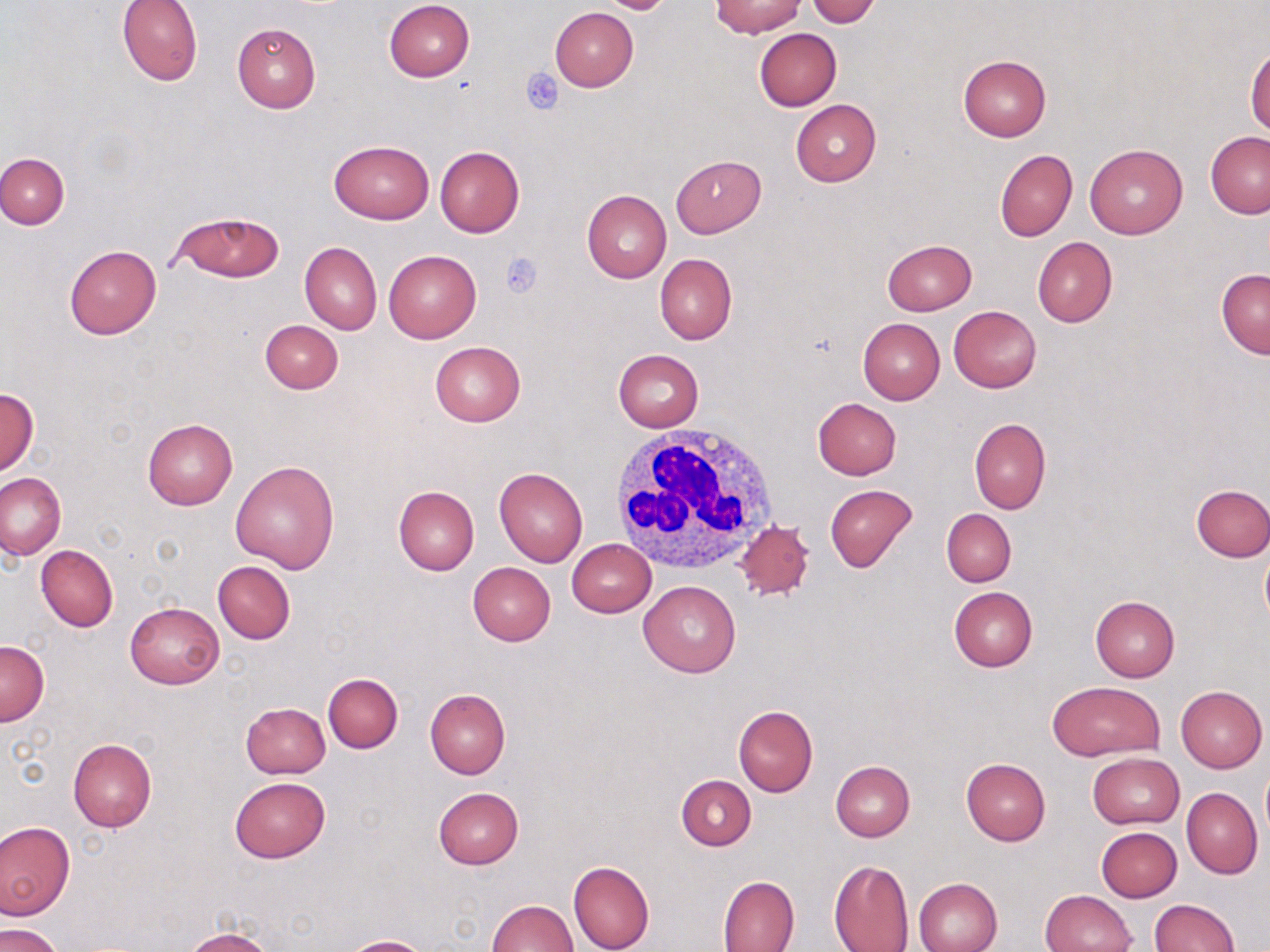

slide-level diagnosis = no evidence of blood parasites
platelet locations = approximate bounding boxes as (x1,y1)-(x2,y2) corner pairs in pixels: (521,68)-(564,114), (497,251)-(543,299)
white blood cell locations = approximate bounding boxes as (x1,y1)-(x2,y2) corner pairs in pixels: (609,422)-(778,579)
preparation = thin blood film
image size = 1270×952 pixels
magnification = 1000x
field of view = single
stain = May-Grünwald-Giemsa
modality = light microscopy
uninfected red blood cell locations = approximate bounding boxes as (x1,y1)-(x2,y2) corner pairs in pixels: (117,0)-(203,85), (595,0)-(677,13), (711,0)-(804,37), (806,0)-(883,27), (384,1)-(475,82), (550,6)-(638,91), (231,21)-(320,114), (754,28)-(841,111), (1245,44)-(1270,137), (957,55)-(1050,142), (791,100)-(881,187), (1205,131)-(1270,218), (329,141)-(433,223), (1086,144)-(1187,239), (435,146)-(524,237), (994,148)-(1076,242), (0,153)-(69,229), (671,155)-(766,237), (582,189)-(671,284), (171,213)-(284,283), (1033,237)-(1117,327), (881,239)-(978,316), (299,241)-(381,334), (64,244)-(162,339), (384,249)-(481,343), (655,254)-(737,344), (1216,269)-(1270,358), (948,306)-(1041,391), (857,319)-(944,404), (260,320)-(343,394), (430,341)-(525,427), (613,348)-(704,431), (0,386)-(38,477), (812,398)-(902,479), (142,418)-(237,510), (969,418)-(1050,514), (230,460)-(339,573), (495,467)-(588,567), (0,472)-(65,559), (824,484)-(917,573), (392,485)-(479,575), (1191,485)-(1270,562), (941,508)-(1017,587), (734,521)-(814,602), (566,538)-(656,617), (35,544)-(118,631), (1260,549)-(1270,627), (213,561)-(296,642), (467,563)-(555,647), (639,581)-(741,678), (948,586)-(1037,672), (1090,596)-(1180,681), (125,601)-(225,689), (0,640)-(49,726), (322,672)-(404,753), (1046,681)-(1165,761), (1176,686)-(1267,772), (424,689)-(511,778), (241,702)-(330,778), (733,705)-(817,797), (68,739)-(157,832), (1087,752)-(1184,828), (960,757)-(1051,846), (831,760)-(915,841), (1262,768)-(1270,843), (230,776)-(330,862), (677,776)-(756,850), (433,787)-(523,870), (1182,787)-(1262,878), (1,821)-(74,918), (1096,826)-(1182,902), (828,858)-(915,952), (567,859)-(653,952), (717,875)-(800,951), (914,877)-(1002,952), (1041,890)-(1136,952), (488,899)-(578,952), (1149,899)-(1239,951), (1,923)-(66,952), (183,929)-(274,952), (341,936)-(432,952)